Locate every blood parasite and identify its species.
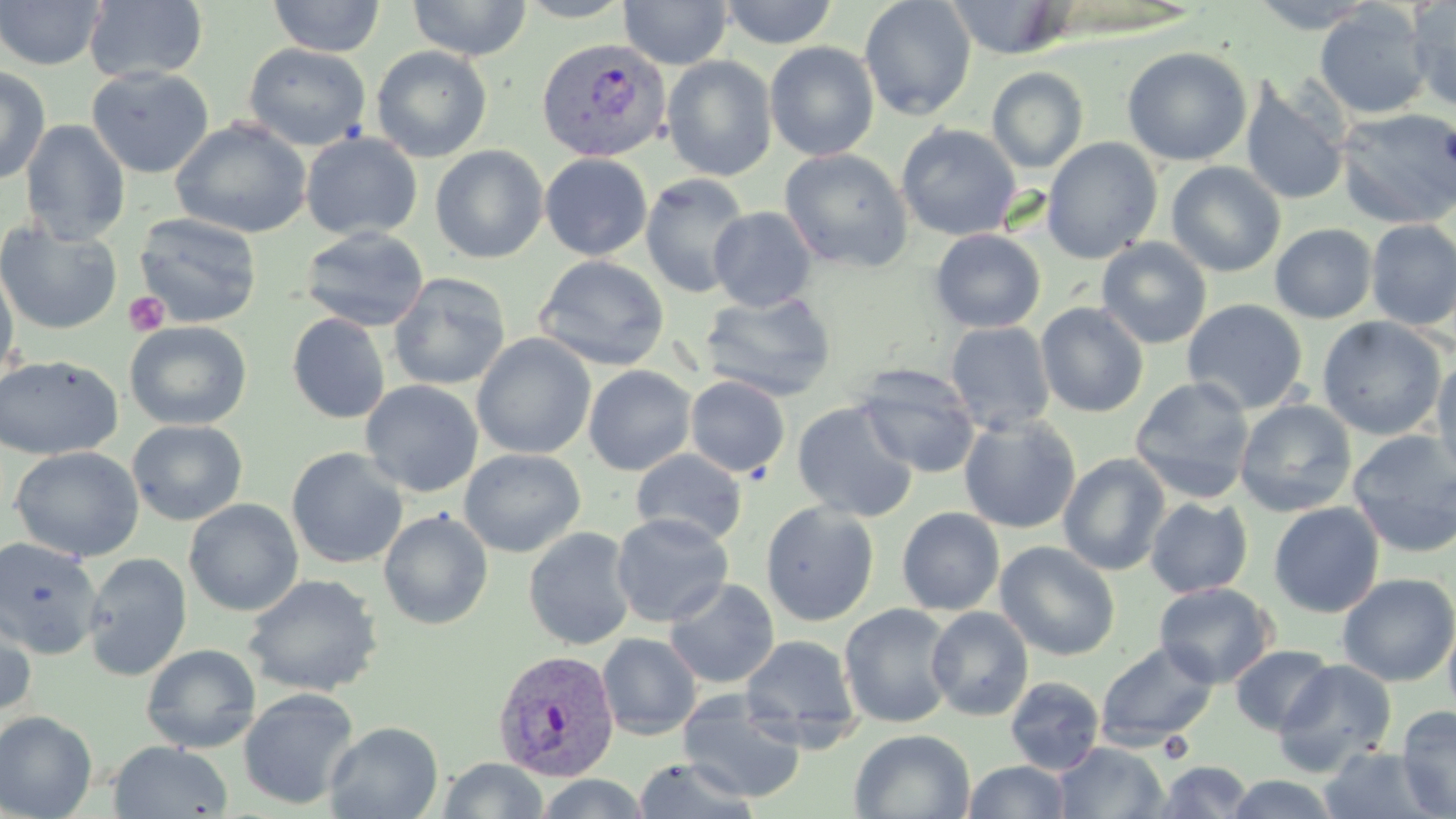

Approximate bounding boxes as [x1, y1, x2, y2] in pixels.
Plasmodium vivax-infected red blood cells: [536, 37, 671, 162], [492, 648, 621, 781].
No Plasmodium falciparum, Plasmodium ovale, Plasmodium malariae, Babesia divergens, or Trypanosoma brucei observed.

slide-level diagnosis = Plasmodium vivax
uninfected red blood cell locations = approximate bounding boxes as [x1, y1, x2, y2] in pixels: [0, 0, 106, 70], [84, 0, 208, 84], [267, 0, 387, 57], [407, 0, 532, 61], [514, 0, 636, 22], [619, 0, 733, 69], [719, 0, 838, 48], [859, 0, 976, 121], [946, 0, 1071, 59], [1247, 0, 1380, 33], [1406, 0, 1456, 110], [1315, 4, 1432, 119], [764, 41, 880, 161], [244, 43, 371, 151], [371, 45, 493, 163], [1121, 47, 1252, 167], [661, 55, 777, 181], [0, 65, 51, 185], [86, 65, 213, 179], [986, 67, 1089, 172], [1240, 76, 1351, 207], [1336, 107, 1456, 229], [171, 117, 312, 239], [20, 119, 131, 245], [896, 123, 1021, 241], [301, 131, 423, 241], [1042, 137, 1163, 264], [430, 144, 549, 263], [779, 148, 913, 272], [539, 153, 653, 260], [1166, 161, 1286, 277], [640, 173, 752, 299], [709, 206, 817, 312], [133, 212, 263, 328], [0, 219, 122, 335], [1365, 220, 1456, 331], [1270, 223, 1377, 324], [299, 226, 429, 332], [929, 229, 1046, 333], [1096, 237, 1212, 349], [534, 255, 669, 371], [0, 263, 19, 383], [388, 272, 511, 391], [699, 290, 837, 402], [1182, 298, 1308, 414], [1035, 302, 1149, 417], [287, 312, 391, 424], [1317, 316, 1447, 441], [124, 321, 253, 431], [944, 321, 1055, 434], [472, 334, 596, 460], [0, 354, 123, 461], [1432, 356, 1456, 484], [583, 365, 697, 475], [854, 365, 982, 478], [685, 375, 791, 478], [1129, 376, 1256, 503], [361, 380, 483, 497], [1234, 399, 1357, 517], [792, 400, 919, 523], [958, 414, 1082, 534], [127, 419, 248, 526], [1346, 429, 1456, 559], [10, 446, 144, 562], [286, 447, 409, 569], [459, 448, 586, 558], [630, 449, 748, 546], [1058, 452, 1172, 576], [1145, 497, 1253, 598], [183, 498, 303, 617], [759, 501, 880, 627], [1268, 502, 1385, 618], [896, 506, 1005, 615], [377, 508, 494, 630], [611, 513, 734, 627], [523, 526, 637, 651], [0, 536, 104, 659], [994, 541, 1121, 661], [83, 552, 192, 680], [1337, 572, 1456, 687], [244, 573, 384, 698], [664, 578, 780, 689], [1153, 582, 1277, 688], [0, 603, 38, 718], [838, 603, 957, 728], [926, 606, 1034, 721], [1442, 612, 1456, 723], [597, 632, 702, 740], [740, 634, 861, 747], [1095, 641, 1220, 751], [141, 643, 261, 753], [1228, 644, 1335, 736], [1273, 659, 1398, 776], [1004, 676, 1105, 775], [238, 687, 360, 810], [677, 690, 808, 803], [1395, 706, 1456, 818], [0, 710, 98, 819], [324, 721, 443, 819], [849, 728, 975, 818], [108, 740, 233, 818], [1053, 742, 1169, 819], [1319, 746, 1443, 818], [437, 757, 549, 818], [632, 757, 761, 818], [963, 760, 1073, 818], [1155, 760, 1255, 817], [533, 773, 651, 818], [1224, 773, 1340, 819]
image size = 1456×819 pixels
platelet locations = approximate bounding boxes as [x1, y1, x2, y2] in pixels: [123, 292, 170, 337]
field of view = one of a larger specimen
stain = May-Grünwald-Giemsa
preparation = thin blood film
magnification = 1000x
modality = light microscopy